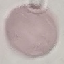

Summary:
  - Result: no malaria parasites seen
  - Stain: Giemsa
  - Preparation: thin blood smear
  - Capture: smartphone camera at the microscope eyepiece
  - Image type: automatically extracted cell patch, resized to 64 × 64 pixels